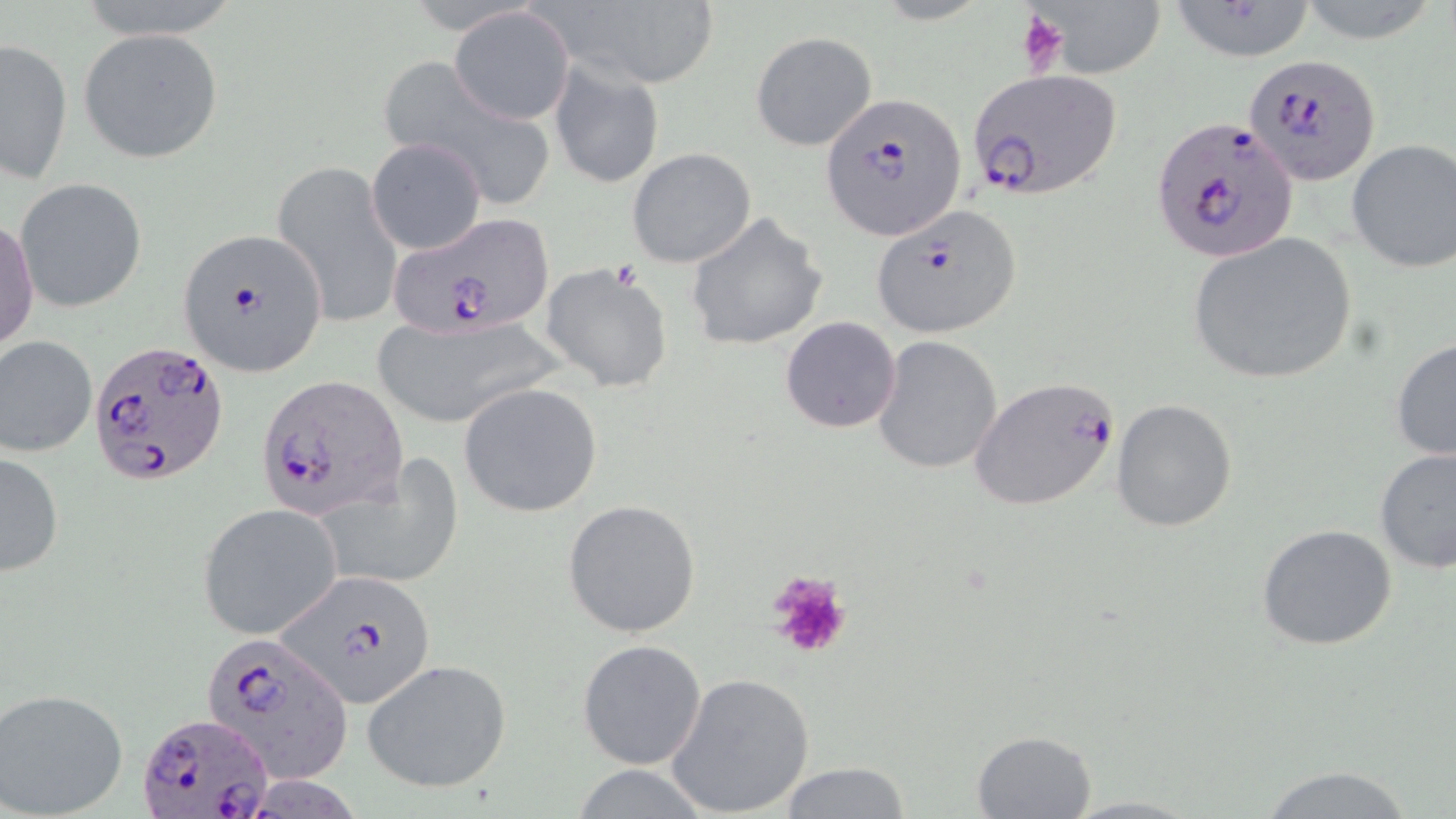
Summary:
  - Coordinate format: approximate bounding boxes as (x1,y1)-(x2,y2) corner pairs in pixels
  - Platelet locations: (1015,9)-(1073,77), (766,571)-(853,660)
  - Plasmodium falciparum-infected red blood cell locations: (1246,53)-(1382,186), (966,69)-(1122,202), (819,92)-(965,239), (1149,115)-(1302,262), (872,206)-(1022,337), (389,215)-(551,335), (175,227)-(328,376), (86,340)-(230,489), (256,374)-(408,518), (969,374)-(1122,511), (279,572)-(439,710), (204,633)-(352,782), (137,710)-(273,819)
  - Uninfected red blood cell locations: (75,0)-(244,40), (1028,0)-(1168,78), (1294,0)-(1447,43), (548,2)-(719,90), (1164,3)-(1321,62), (451,7)-(574,126), (78,28)-(225,164), (750,30)-(877,151), (1,37)-(73,184), (547,58)-(663,189), (377,60)-(555,208), (368,138)-(486,254), (1346,138)-(1456,273), (626,147)-(757,268), (272,161)-(404,328), (14,179)-(147,312), (682,211)-(827,353), (1,216)-(38,355), (1186,233)-(1358,385), (540,262)-(675,394), (369,315)-(560,427), (779,316)-(902,433), (0,334)-(97,458), (871,335)-(1004,474), (1391,337)-(1456,463), (458,381)-(604,518), (1112,398)-(1238,535), (1374,446)-(1455,573), (1,449)-(64,576), (313,458)-(464,593), (562,499)-(701,637), (199,505)-(342,639), (1258,524)-(1398,650), (577,638)-(707,769), (362,658)-(512,793), (665,672)-(816,816), (0,688)-(130,817), (972,729)-(1097,817), (774,761)-(916,817), (1253,763)-(1421,819), (563,764)-(719,818), (1058,793)-(1208,818)
  - Slide-level diagnosis: Plasmodium falciparum
  - Image size: 1456×819 pixels
  - Modality: optical microscopy
  - Field of view: one of a larger specimen
  - Magnification: 1000x
  - Stain: May-Grünwald-Giemsa
  - Preparation: thin blood film